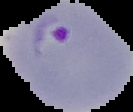

Segmented cell region on a black background. From a thin blood film. Malaria status: parasitized. Image is 133×112 pixels.